Describe the morphology of the red blood cells.
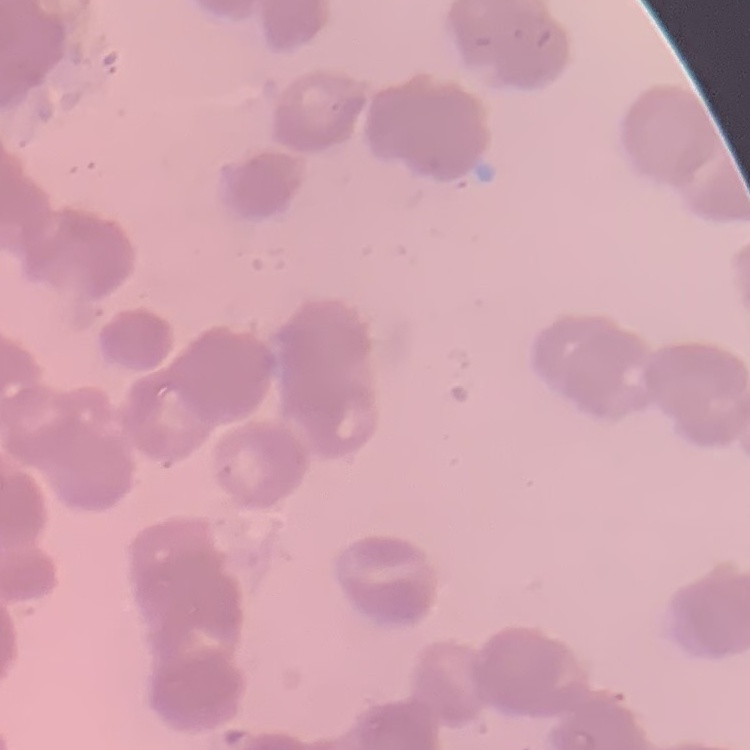
They show rouleaux formation.

preparation: thin blood film
image_type: one tile cut from a larger photomicrograph
stain: Field's or Giemsa